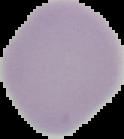

Result: no malaria parasites seen. From a thin blood smear. Image is 124×139 pixels. The area outside the segmented cell region is set to black.